Outline each blood parasite and name the species.
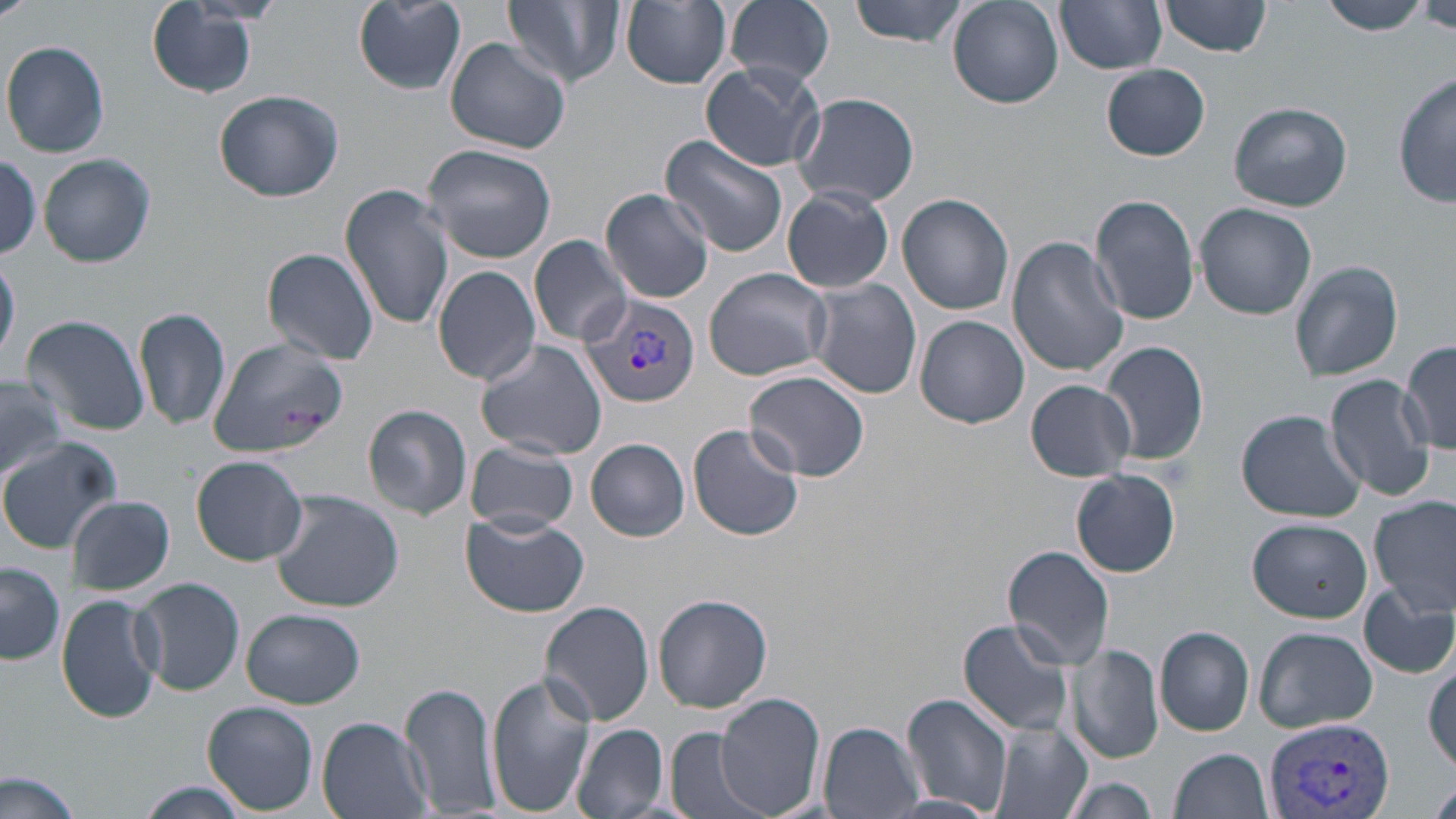
Approximate bounding boxes as [x1, y1, x2, y2] in pixels.
Plasmodium vivax-infected red blood cells: [581, 292, 700, 408], [1262, 714, 1402, 819].
No Plasmodium falciparum, Plasmodium ovale, Plasmodium malariae, Babesia divergens, or Trypanosoma brucei observed.

Uninfected red blood cell locations: [0, 0, 39, 21], [349, 0, 469, 96], [504, 0, 624, 90], [724, 0, 836, 88], [846, 0, 973, 47], [1058, 0, 1166, 74], [1159, 0, 1272, 57], [1317, 0, 1431, 35], [621, 1, 732, 89], [147, 2, 264, 99], [948, 2, 1064, 108], [1418, 4, 1456, 37], [444, 37, 571, 155], [2, 40, 110, 158], [700, 60, 827, 172], [1102, 63, 1210, 160], [1393, 74, 1454, 210], [215, 89, 344, 202], [792, 94, 920, 209], [1230, 103, 1352, 211], [660, 134, 789, 259], [422, 142, 556, 263], [0, 152, 45, 263], [39, 154, 155, 268], [340, 184, 457, 334], [782, 187, 894, 295], [600, 188, 715, 303], [897, 192, 1014, 316], [1089, 194, 1200, 325], [1194, 202, 1317, 320], [529, 234, 633, 348], [1005, 234, 1128, 378], [261, 247, 380, 366], [0, 254, 20, 370], [1290, 258, 1405, 383], [433, 265, 541, 388], [704, 267, 832, 382], [808, 277, 922, 399], [133, 306, 232, 432], [22, 314, 150, 436], [914, 315, 1029, 429], [209, 332, 341, 455], [475, 337, 608, 461], [1399, 339, 1456, 458], [1099, 340, 1210, 469], [744, 371, 872, 483], [1, 373, 66, 484], [1325, 375, 1435, 502], [1026, 380, 1136, 481], [364, 404, 472, 519], [1236, 410, 1367, 524], [687, 423, 805, 541], [0, 437, 123, 552], [586, 438, 689, 541], [463, 442, 579, 533], [190, 455, 308, 566], [1071, 469, 1180, 578], [268, 487, 407, 612], [65, 495, 176, 595], [1368, 496, 1456, 620], [460, 512, 587, 617], [1248, 518, 1372, 624], [1004, 546, 1117, 669], [1, 562, 66, 666], [133, 577, 245, 696], [1358, 582, 1455, 680], [55, 592, 164, 723], [654, 594, 773, 713], [539, 601, 655, 725], [241, 608, 364, 709], [957, 618, 1074, 738], [1155, 625, 1255, 735], [1253, 627, 1377, 733], [1069, 645, 1165, 765], [485, 671, 596, 818], [401, 683, 502, 817], [899, 693, 1014, 819], [714, 694, 825, 819], [203, 702, 319, 814], [316, 715, 434, 819], [818, 722, 924, 818], [989, 722, 1091, 819], [570, 723, 670, 819], [665, 727, 766, 819], [1172, 749, 1273, 819], [0, 769, 86, 819], [1059, 777, 1162, 818], [134, 780, 258, 818], [1425, 783, 1456, 819]. Slide-level diagnosis: Plasmodium vivax. Single field of view. Image is 1456×819 pixels. Thin blood smear. May-Grünwald-Giemsa-stained preparation. Optical microscopy. Captured at 1000x magnification.